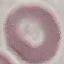
Malaria status: uninfected. Cell patch, automatically extracted from a larger field of view and resized to 64 × 64 pixels. Giemsa-stained preparation. Thin blood film. Photographed with a smartphone camera at the microscope eyepiece.